Comment on the morphology of the erythrocytes.
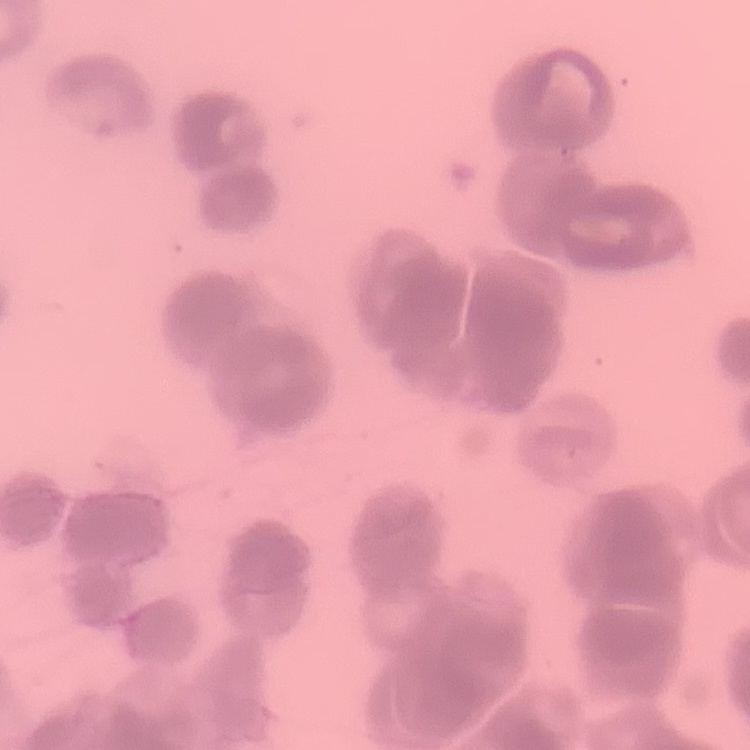

Rouleaux formation.

Summary:
  - Stain: Field's or Giemsa
  - Image type: one tile cut from a larger photomicrograph
  - Preparation: thin blood smear